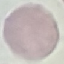

Summary:
  - Malaria status: uninfected
  - Stain: Giemsa
  - Image type: automatically extracted cell patch, resized to 64 × 64 pixels
  - Preparation: thin smear
  - Capture: smartphone through the microscope eyepiece